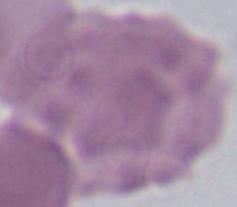
Summary:
  - Magnification: 1000x
  - Identification: erythrocyte
  - Modality: micrograph